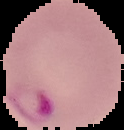

preparation: thin blood film
image_type: segmented cell region with the area outside set to black
malaria_status: parasitized
image_size: 124×130 pixels